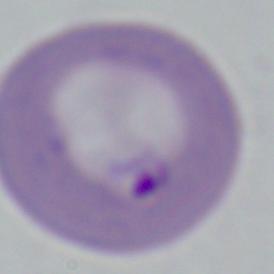
Summary:
  - Magnification: 1000x
  - Identification: Babesia
  - Modality: photomicrograph